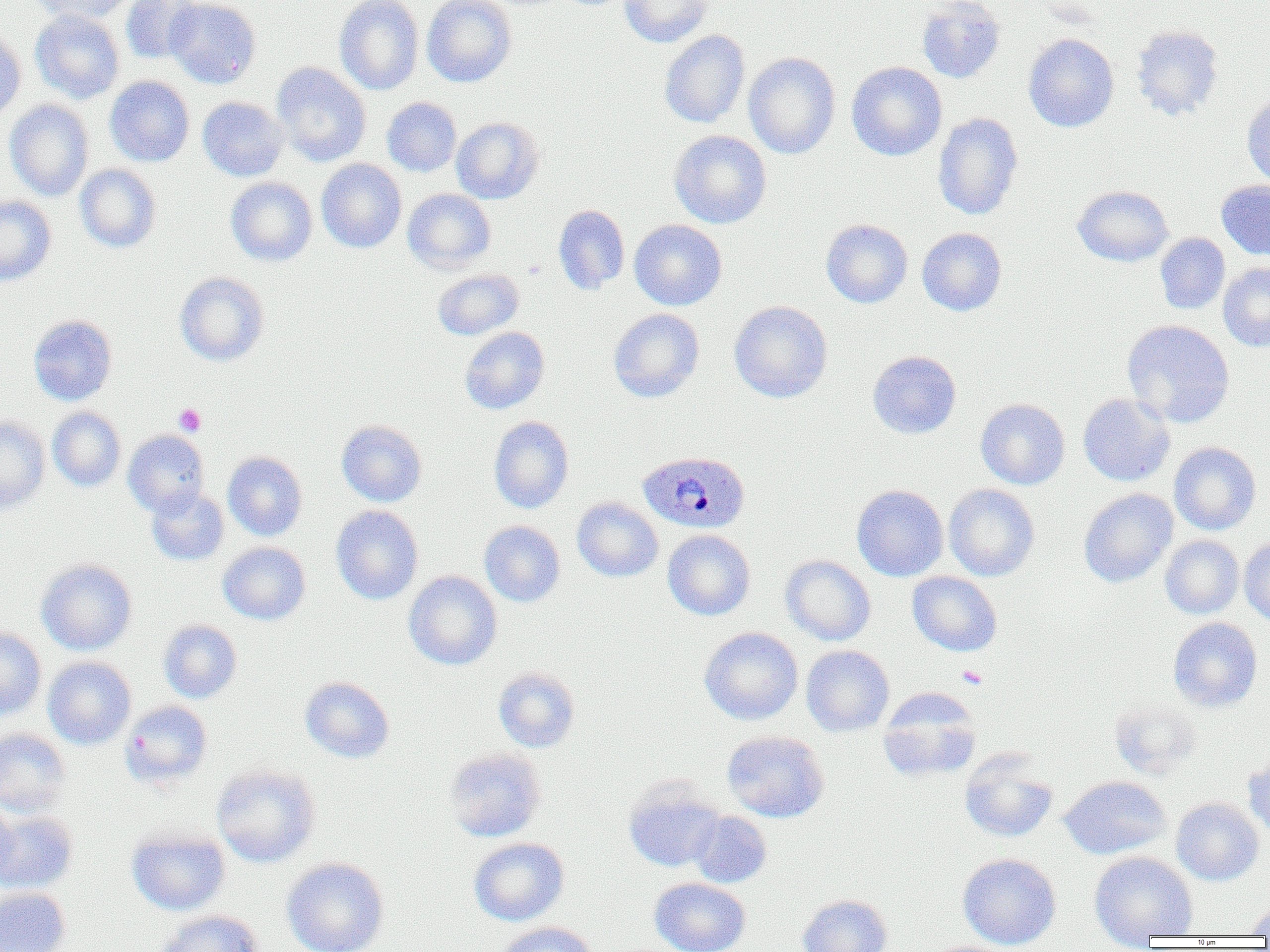

Summary:
  - Coordinate format: approximate bounding boxes as (x1,y1)-(x2,y2) corner pairs in pixels
  - Uninfected red blood cell locations: (29,0)-(135,24), (121,0)-(204,64), (165,0)-(261,88), (335,0)-(424,95), (422,0)-(517,87), (619,0)-(712,47), (916,0)-(1006,83), (30,10)-(125,103), (1130,25)-(1224,121), (0,26)-(26,123), (659,30)-(750,129), (1023,33)-(1119,132), (743,52)-(841,159), (272,62)-(371,166), (846,62)-(947,160), (105,76)-(195,167), (1242,95)-(1270,189), (197,96)-(288,181), (382,97)-(461,177), (5,99)-(94,201), (933,113)-(1023,220), (451,117)-(544,204), (668,130)-(772,229), (316,159)-(406,253), (74,164)-(162,252), (226,177)-(317,266), (1217,180)-(1270,260), (1072,185)-(1174,266), (402,188)-(496,274), (0,196)-(57,285), (553,205)-(630,294), (629,219)-(727,310), (821,219)-(913,308), (917,228)-(1007,316), (1155,233)-(1230,314), (1218,262)-(1270,352), (432,269)-(523,340), (173,272)-(270,366), (729,300)-(833,402), (608,308)-(704,402), (28,315)-(117,405), (43,315)-(122,491), (1121,319)-(1235,428), (459,327)-(550,414), (867,350)-(961,438), (1077,393)-(1175,486), (976,398)-(1070,490), (47,406)-(126,491), (0,416)-(50,513), (488,416)-(574,513), (336,420)-(427,507), (123,429)-(209,517), (1169,442)-(1262,535), (223,451)-(308,541), (943,484)-(1040,581), (852,485)-(949,581), (146,487)-(229,566), (1078,488)-(1178,588), (572,497)-(663,582), (331,505)-(423,604), (479,520)-(565,607), (662,530)-(756,620), (1160,535)-(1244,619), (1239,537)-(1270,625), (218,541)-(310,624), (780,555)-(876,646), (37,559)-(136,655), (404,571)-(502,670), (907,571)-(1002,656), (1168,617)-(1263,712), (158,620)-(242,703), (0,627)-(46,720), (699,627)-(803,725), (801,645)-(894,737), (43,656)-(136,750), (493,666)-(581,753), (299,676)-(394,763), (877,688)-(981,782), (1108,696)-(1203,780), (120,701)-(212,789), (0,728)-(71,816), (722,730)-(830,822), (444,748)-(546,842), (959,749)-(1058,842), (1243,753)-(1270,838), (211,764)-(320,867), (1059,776)-(1171,859), (623,780)-(724,872), (1171,797)-(1264,885), (0,800)-(19,889), (0,811)-(78,894), (689,811)-(772,888), (126,827)-(231,915), (468,837)-(569,926), (1089,850)-(1198,948), (958,853)-(1061,950), (281,857)-(390,952), (650,877)-(751,952), (0,887)-(71,952), (797,894)-(893,952), (1243,905)-(1270,935), (154,909)-(265,952), (497,921)-(597,952)
  - Platelet locations: (174,403)-(206,436), (957,666)-(988,689)
  - Plasmodium ovale-infected red blood cell locations: (636,451)-(751,534)
  - Slide-level diagnosis: Plasmodium ovale
  - Magnification: 1000x
  - Modality: optical microscopy
  - Field of view: single
  - Image size: 1270×952 pixels
  - Preparation: thin blood film